Name the parasite shown.
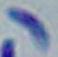
This is Toxoplasma gondii.

modality = photomicrograph
magnification = 1000x